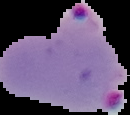 Image is 130×115 pixels. Malaria status: parasitized. Cell region segmented out of the field of view; the surrounding area is masked to black. From a thin blood film.